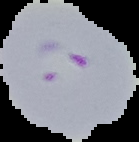
Summary:
  - Malaria status: parasitized
  - Preparation: thin blood smear
  - Image type: segmented cell region on a black background
  - Image size: 139×142 pixels